Assess this cell for malaria.
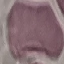

It is uninfected.

capture = smartphone camera at the microscope eyepiece
stain = Giemsa
image type = automatically extracted cell patch, resized to 64 × 64 pixels
preparation = thin smear